Locate every blood parasite and identify its species.
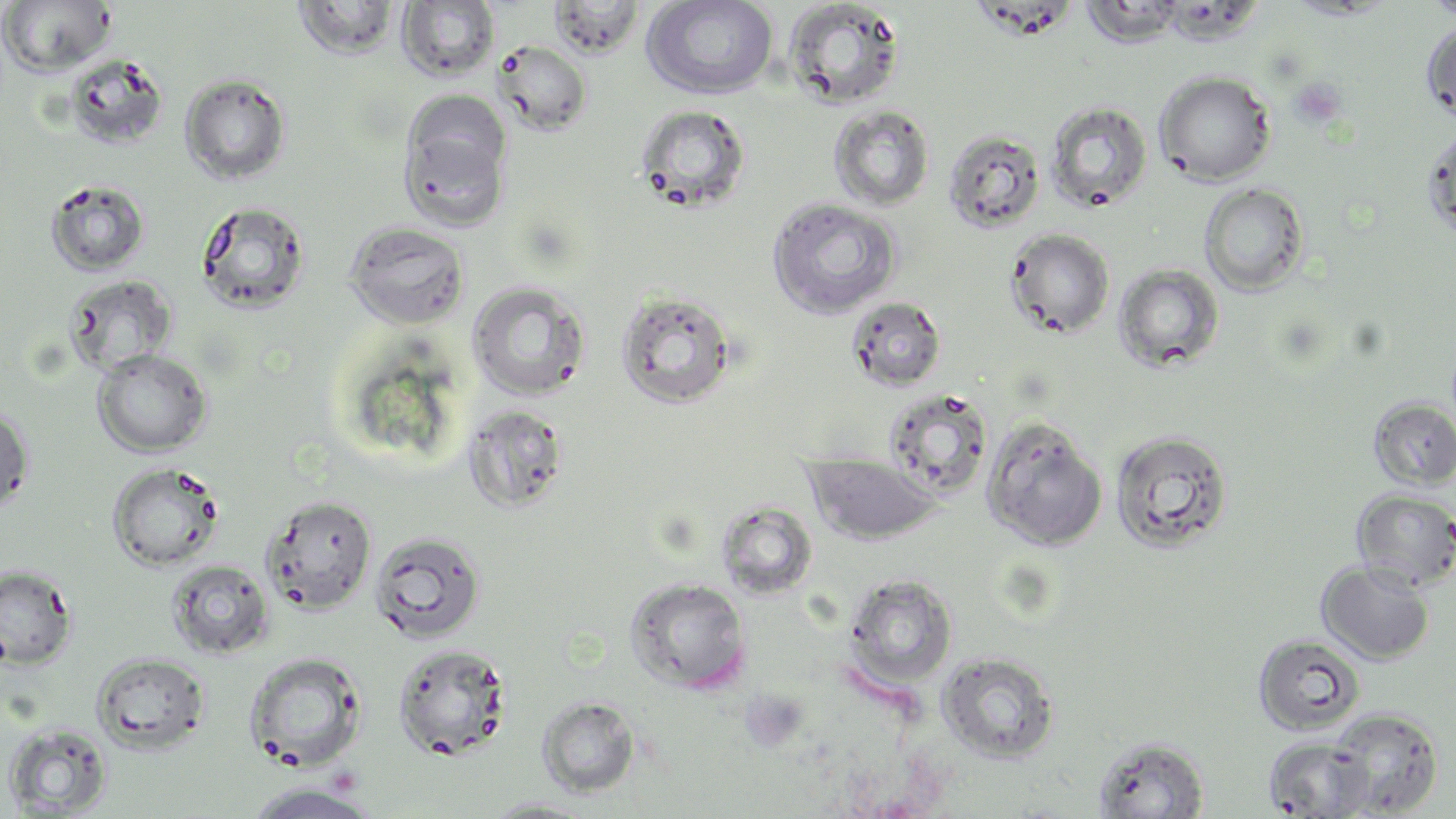

No blood parasites observed.

Approximate bounding boxes as named x1/y1/x2/y2 corners in pixels. Uninfected red blood cell locations: (x1=292, y1=0, x2=401, y2=59), (x1=547, y1=0, x2=645, y2=59), (x1=641, y1=0, x2=779, y2=100), (x1=781, y1=0, x2=907, y2=110), (x1=1421, y1=0, x2=1456, y2=22), (x1=0, y1=1, x2=116, y2=77), (x1=397, y1=1, x2=500, y2=82), (x1=1080, y1=1, x2=1188, y2=48), (x1=1421, y1=17, x2=1456, y2=126), (x1=492, y1=40, x2=592, y2=136), (x1=63, y1=53, x2=169, y2=149), (x1=1154, y1=71, x2=1276, y2=186), (x1=179, y1=73, x2=292, y2=185), (x1=398, y1=96, x2=512, y2=228), (x1=1045, y1=100, x2=1153, y2=213), (x1=633, y1=103, x2=752, y2=214), (x1=828, y1=105, x2=935, y2=211), (x1=1422, y1=122, x2=1456, y2=243), (x1=943, y1=128, x2=1046, y2=234), (x1=45, y1=179, x2=151, y2=277), (x1=1199, y1=183, x2=1310, y2=295), (x1=767, y1=198, x2=902, y2=320), (x1=195, y1=200, x2=311, y2=314), (x1=344, y1=221, x2=470, y2=330), (x1=1005, y1=228, x2=1115, y2=339), (x1=1113, y1=263, x2=1225, y2=373), (x1=63, y1=274, x2=178, y2=377), (x1=466, y1=281, x2=592, y2=400), (x1=614, y1=290, x2=739, y2=409), (x1=846, y1=296, x2=947, y2=391), (x1=92, y1=349, x2=212, y2=457), (x1=883, y1=388, x2=994, y2=499), (x1=1368, y1=397, x2=1456, y2=490), (x1=461, y1=402, x2=571, y2=514), (x1=0, y1=404, x2=35, y2=517), (x1=981, y1=416, x2=1108, y2=550), (x1=1110, y1=430, x2=1234, y2=553), (x1=803, y1=453, x2=943, y2=545), (x1=107, y1=462, x2=224, y2=572), (x1=1352, y1=489, x2=1456, y2=591), (x1=261, y1=494, x2=377, y2=615), (x1=715, y1=500, x2=819, y2=599), (x1=369, y1=530, x2=487, y2=644), (x1=166, y1=559, x2=275, y2=659), (x1=1317, y1=560, x2=1435, y2=664), (x1=0, y1=564, x2=77, y2=668), (x1=844, y1=574, x2=958, y2=689), (x1=625, y1=577, x2=752, y2=694), (x1=1253, y1=633, x2=1365, y2=736), (x1=392, y1=643, x2=513, y2=761), (x1=936, y1=651, x2=1061, y2=762), (x1=244, y1=652, x2=367, y2=772), (x1=91, y1=653, x2=210, y2=754), (x1=537, y1=696, x2=640, y2=798), (x1=1328, y1=708, x2=1444, y2=816), (x1=3, y1=722, x2=114, y2=816), (x1=1092, y1=736, x2=1210, y2=818), (x1=1263, y1=736, x2=1375, y2=817), (x1=241, y1=783, x2=382, y2=818), (x1=480, y1=797, x2=601, y2=818). Slide-level diagnosis: no evidence of blood parasites. Image is 1456×819 pixels. Optical microscopy. Captured at 1000x magnification. May-Grünwald-Giemsa stain. Single field of view. Thin blood film.